Point out each leukocyte.
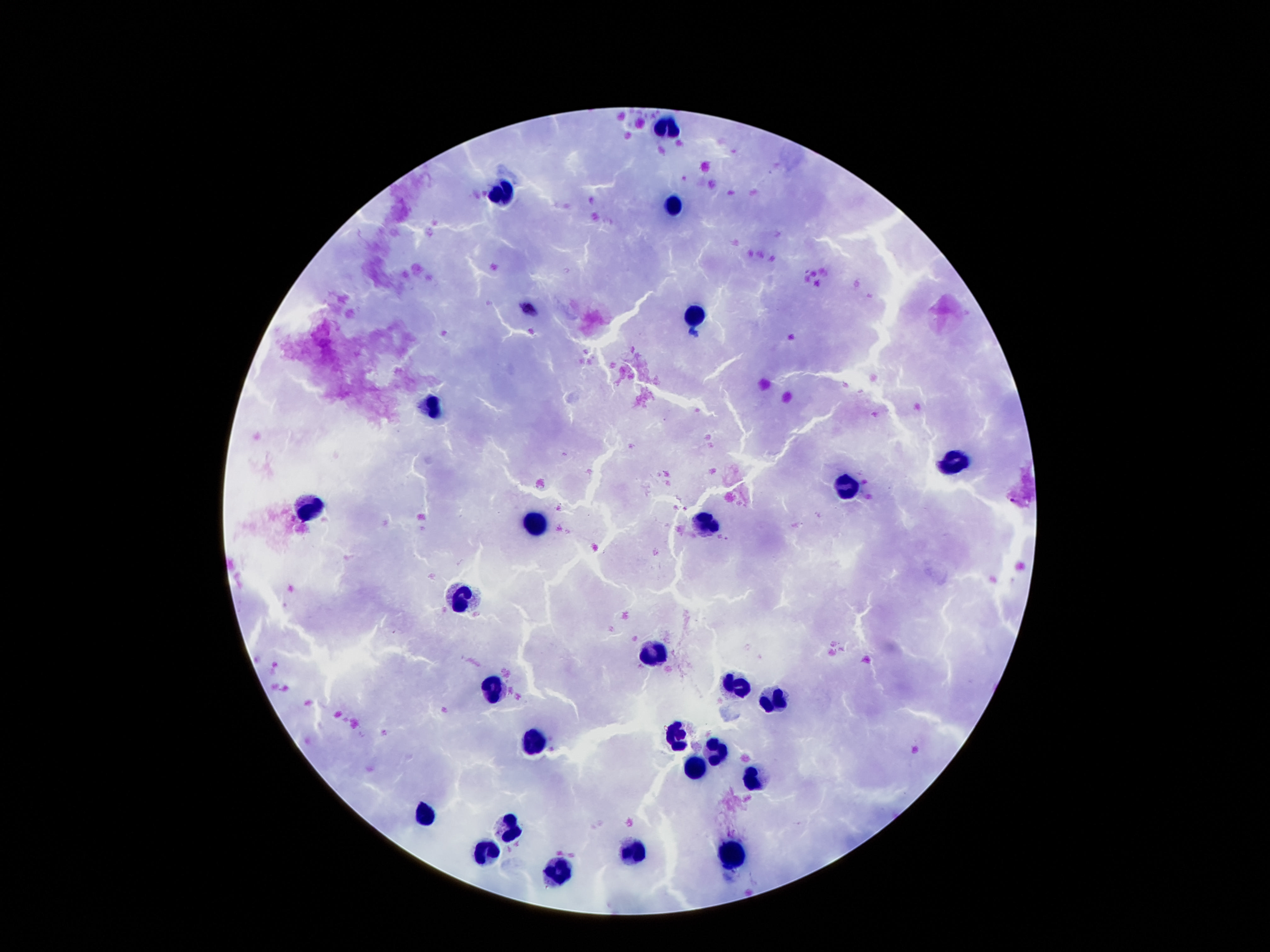
Approximate centers as [x, y] in pixels.
Leukocytes: [666, 127], [503, 194], [674, 206], [695, 316], [434, 406], [954, 462], [847, 488], [312, 506], [537, 524], [704, 525], [463, 599], [655, 654], [737, 688], [493, 691], [773, 704], [678, 735], [527, 743], [716, 753], [695, 767], [752, 779], [426, 814], [508, 829], [634, 851], [733, 853], [484, 856], [556, 875].

stain = Giemsa
capture = smartphone camera through the microscope eyepiece
preparation = thick peripheral-blood smear
patient malaria status = uninfected
magnification = 100x
field of view = one from this slide
image size = 1270×952 pixels